Point out each Plasmodium parasite.
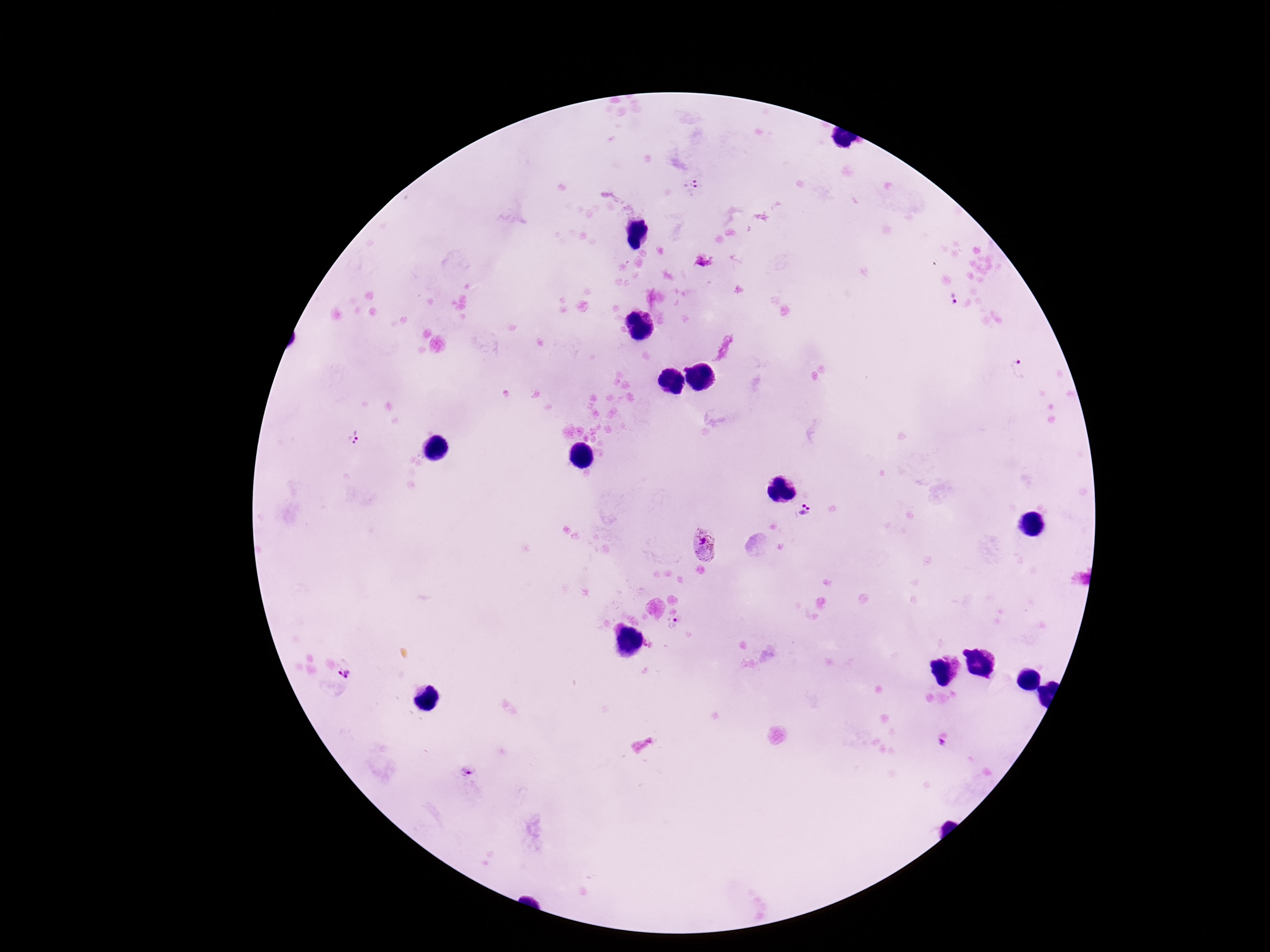

Approximate centers as (x, y) in pixels.
Plasmodium parasites: (692, 185), (953, 298), (1020, 369), (354, 438), (805, 512), (705, 546), (675, 625), (346, 673), (943, 742), (469, 772).

Summary:
  - Preparation: thick blood film
  - Capture: smartphone camera through the microscope eyepiece
  - Stain: Giemsa
  - Field of view: single
  - Image size: 1270×952 pixels
  - Patient malaria status: positive
  - Magnification: 100x